Point out each Plasmodium parasite.
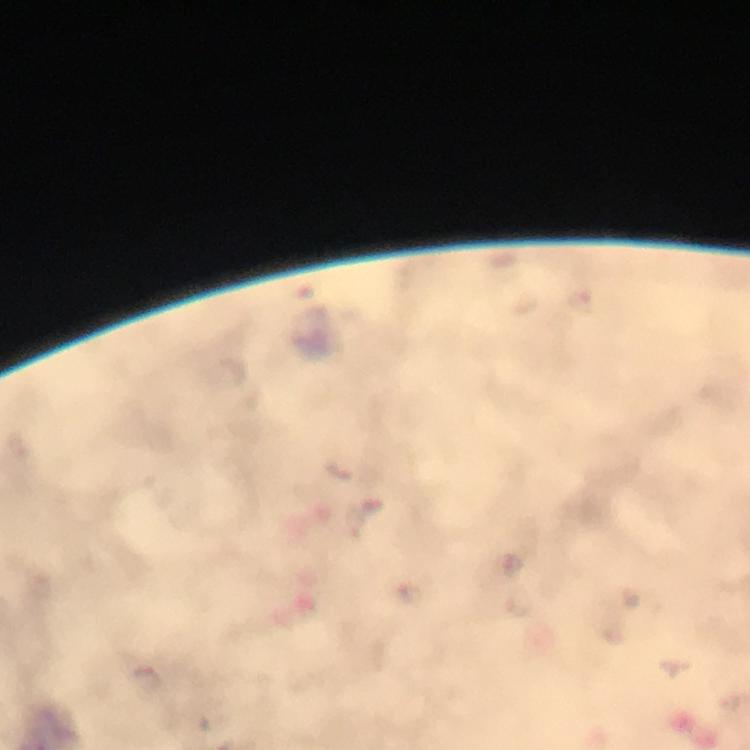

Approximate object centers, in pixels from the top-left corner.
Plasmodium parasites: (x=145, y=678).

Summary:
  - Cropped from: a single field of view
  - Stain: Giemsa
  - Context: from a malaria diagnostic workup
  - Magnification: 100x
  - Image size: 750×750 pixels
  - Preparation: thick blood film
  - Capture: smartphone mounted on the microscope
  - Immersion oil: applied